Give the extent of all Plasmodium ovale-infected red blood cells.
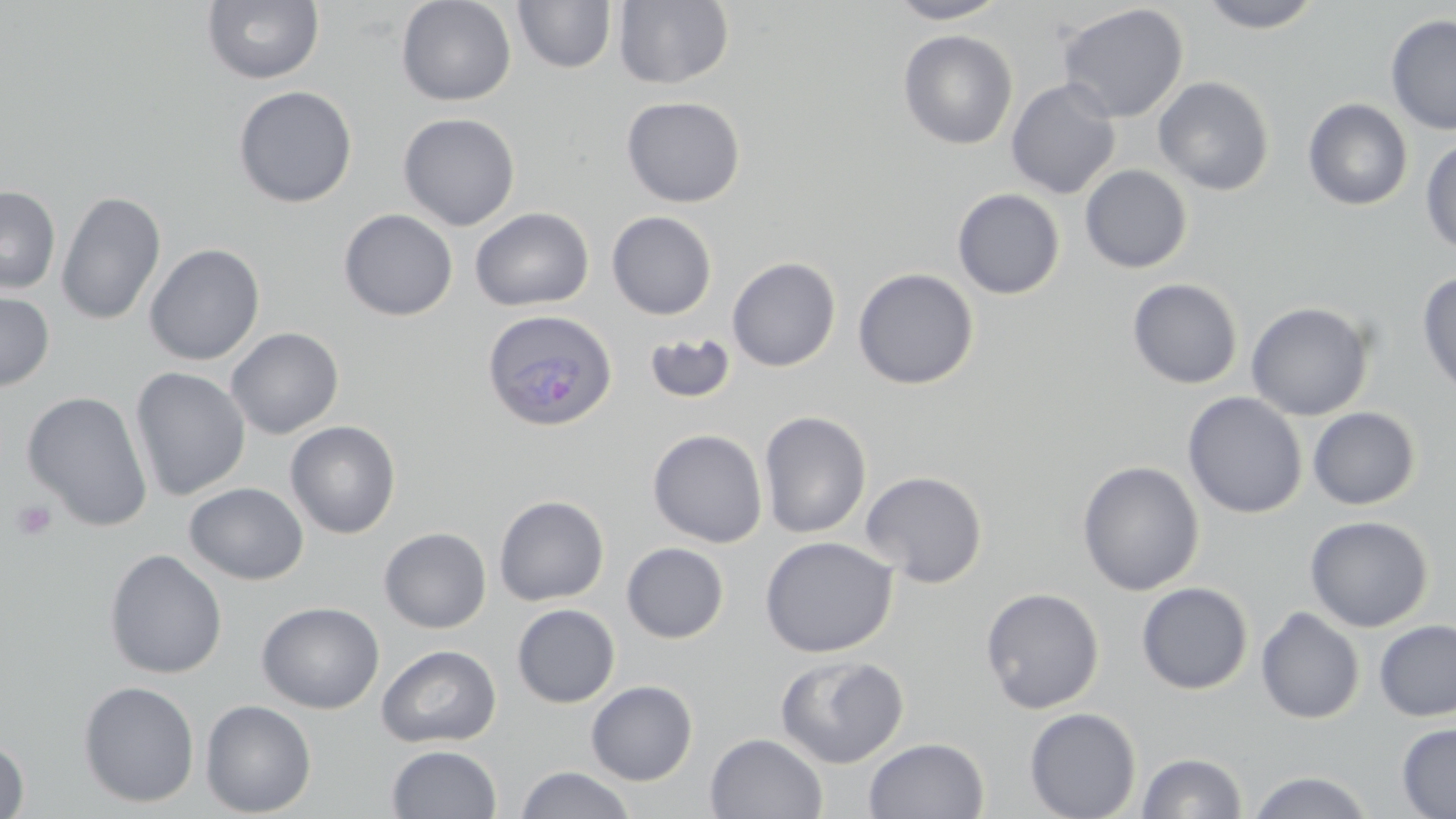
Approximate bounding boxes as named x1/y1/x2/y2 corners in pixels.
Plasmodium ovale-infected red blood cells: (x1=482, y1=310, x2=617, y2=432).

slide-level diagnosis = Plasmodium ovale
modality = optical microscopy
magnification = 1000x
field of view = single
image size = 1456×819 pixels
preparation = thin blood film
platelet locations = approximate bounding boxes as named x1/y1/x2/y2 corners in pixels: (x1=11, y1=499, x2=58, y2=542)
uninfected red blood cell locations = approximate bounding boxes as named x1/y1/x2/y2 corners in pixels: (x1=395, y1=0, x2=517, y2=107), (x1=613, y1=0, x2=735, y2=90), (x1=887, y1=0, x2=1009, y2=24), (x1=1196, y1=0, x2=1325, y2=33), (x1=202, y1=1, x2=325, y2=85), (x1=512, y1=1, x2=616, y2=74), (x1=1057, y1=3, x2=1189, y2=123), (x1=1385, y1=14, x2=1456, y2=135), (x1=898, y1=30, x2=1018, y2=150), (x1=1153, y1=76, x2=1275, y2=196), (x1=1006, y1=78, x2=1121, y2=200), (x1=233, y1=85, x2=358, y2=208), (x1=621, y1=95, x2=746, y2=208), (x1=1302, y1=98, x2=1414, y2=211), (x1=398, y1=112, x2=520, y2=231), (x1=1420, y1=137, x2=1456, y2=257), (x1=1080, y1=165, x2=1192, y2=273), (x1=0, y1=186, x2=61, y2=294), (x1=952, y1=188, x2=1065, y2=299), (x1=56, y1=191, x2=166, y2=326), (x1=470, y1=207, x2=594, y2=311), (x1=339, y1=209, x2=459, y2=321), (x1=607, y1=211, x2=717, y2=320), (x1=143, y1=243, x2=265, y2=365), (x1=726, y1=256, x2=841, y2=372), (x1=852, y1=267, x2=980, y2=390), (x1=1417, y1=269, x2=1456, y2=399), (x1=1127, y1=278, x2=1244, y2=389), (x1=0, y1=289, x2=55, y2=392), (x1=1246, y1=301, x2=1374, y2=421), (x1=226, y1=327, x2=344, y2=439), (x1=643, y1=332, x2=736, y2=405), (x1=130, y1=367, x2=250, y2=501), (x1=21, y1=391, x2=153, y2=531), (x1=1183, y1=392, x2=1308, y2=519), (x1=1307, y1=406, x2=1421, y2=510), (x1=758, y1=410, x2=872, y2=539), (x1=284, y1=420, x2=401, y2=539), (x1=647, y1=428, x2=768, y2=548), (x1=1077, y1=460, x2=1205, y2=595), (x1=861, y1=470, x2=988, y2=588), (x1=184, y1=482, x2=308, y2=585), (x1=493, y1=494, x2=609, y2=606), (x1=1304, y1=515, x2=1433, y2=632), (x1=379, y1=527, x2=491, y2=633), (x1=760, y1=535, x2=898, y2=658), (x1=621, y1=542, x2=729, y2=644), (x1=104, y1=549, x2=227, y2=679), (x1=1136, y1=582, x2=1254, y2=695), (x1=980, y1=586, x2=1105, y2=714), (x1=256, y1=601, x2=384, y2=714), (x1=512, y1=603, x2=620, y2=708), (x1=1255, y1=606, x2=1365, y2=724), (x1=1373, y1=619, x2=1456, y2=722), (x1=376, y1=644, x2=501, y2=748), (x1=775, y1=653, x2=909, y2=769), (x1=78, y1=680, x2=199, y2=808), (x1=585, y1=680, x2=698, y2=785), (x1=200, y1=699, x2=317, y2=817), (x1=1024, y1=707, x2=1142, y2=819), (x1=1397, y1=722, x2=1456, y2=818), (x1=705, y1=732, x2=829, y2=819), (x1=0, y1=736, x2=30, y2=819), (x1=863, y1=736, x2=990, y2=819), (x1=386, y1=744, x2=502, y2=818), (x1=1137, y1=752, x2=1247, y2=818), (x1=515, y1=766, x2=637, y2=819), (x1=1246, y1=770, x2=1375, y2=818)
stain = May-Grünwald-Giemsa